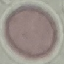
Summary:
  - Result: no malaria parasites detected
  - Preparation: thin blood smear
  - Stain: Giemsa
  - Image type: automatically extracted cell patch, resized to 64 × 64 pixels
  - Capture: smartphone camera at the microscope eyepiece